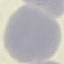

malaria status = uninfected
image type = automatically extracted cell patch, resized to 64 × 64 pixels
preparation = thin blood film
stain = Giemsa
capture = smartphone through the microscope eyepiece